Locate platelets.
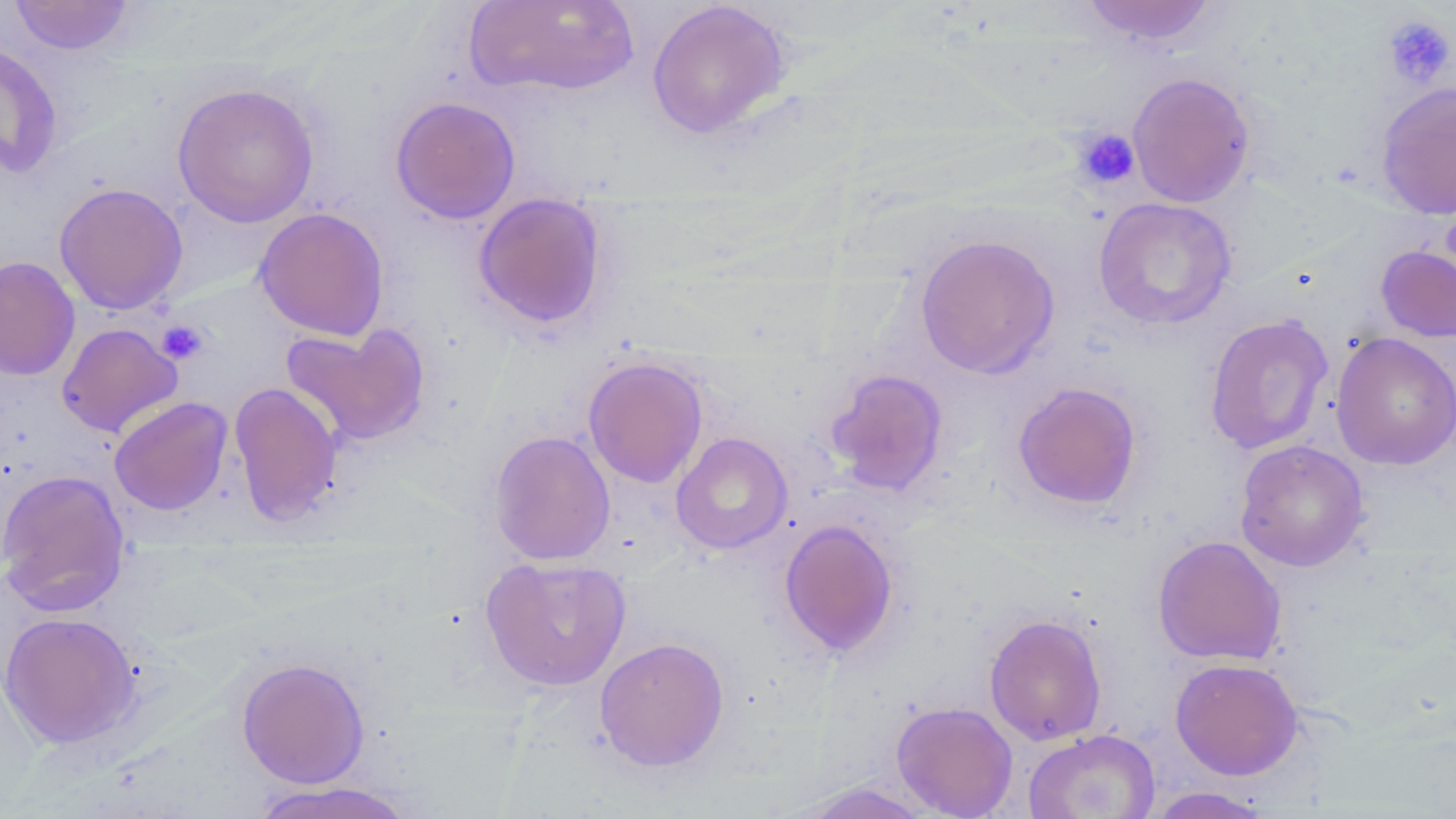
Approximate bounding boxes as named x1/y1/x2/y2 corners in pixels.
Platelets: (x1=1381, y1=14, x2=1455, y2=89), (x1=1073, y1=127, x2=1141, y2=190), (x1=156, y1=319, x2=209, y2=365).

slide-level diagnosis = no evidence of blood parasites
uninfected red blood cell locations = approximate bounding boxes as named x1/y1/x2/y2 corners in pixels: (x1=8, y1=0, x2=135, y2=55), (x1=463, y1=0, x2=641, y2=99), (x1=1078, y1=0, x2=1221, y2=47), (x1=646, y1=1, x2=792, y2=139), (x1=0, y1=41, x2=64, y2=180), (x1=1127, y1=72, x2=1256, y2=208), (x1=1375, y1=81, x2=1456, y2=221), (x1=171, y1=82, x2=320, y2=228), (x1=390, y1=96, x2=521, y2=224), (x1=53, y1=182, x2=189, y2=315), (x1=472, y1=193, x2=609, y2=333), (x1=1093, y1=197, x2=1238, y2=330), (x1=254, y1=207, x2=390, y2=341), (x1=914, y1=233, x2=1060, y2=379), (x1=1375, y1=244, x2=1456, y2=343), (x1=0, y1=256, x2=80, y2=382), (x1=1204, y1=314, x2=1335, y2=455), (x1=56, y1=322, x2=183, y2=438), (x1=280, y1=322, x2=431, y2=447), (x1=1331, y1=333, x2=1456, y2=471), (x1=583, y1=357, x2=708, y2=487), (x1=825, y1=368, x2=949, y2=497), (x1=229, y1=380, x2=343, y2=526), (x1=1011, y1=381, x2=1143, y2=511), (x1=108, y1=396, x2=233, y2=516), (x1=488, y1=430, x2=615, y2=565), (x1=671, y1=432, x2=793, y2=555), (x1=1234, y1=440, x2=1370, y2=573), (x1=0, y1=469, x2=131, y2=616), (x1=778, y1=519, x2=900, y2=658), (x1=1151, y1=535, x2=1287, y2=665), (x1=479, y1=556, x2=631, y2=691), (x1=0, y1=611, x2=142, y2=748), (x1=984, y1=612, x2=1107, y2=745), (x1=594, y1=636, x2=730, y2=772), (x1=235, y1=656, x2=371, y2=788), (x1=1170, y1=658, x2=1303, y2=780), (x1=891, y1=701, x2=1018, y2=818), (x1=1023, y1=728, x2=1160, y2=819), (x1=245, y1=780, x2=419, y2=819), (x1=787, y1=781, x2=936, y2=818), (x1=1144, y1=786, x2=1275, y2=818)
image size = 1456×819 pixels
stain = May-Grünwald-Giemsa
field of view = one of a larger specimen
modality = optical microscopy
magnification = 1000x
preparation = thin blood smear